Report the malaria status of this cell.
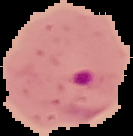

It is parasitized.

Summary:
  - Preparation: thin blood film
  - Image size: 133×136 pixels
  - Image type: segmented cell region with the area outside set to black